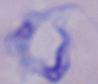

A trypanosome is seen. Photomicrograph. 1000x magnification.